Assess the morphology of the erythrocytes.
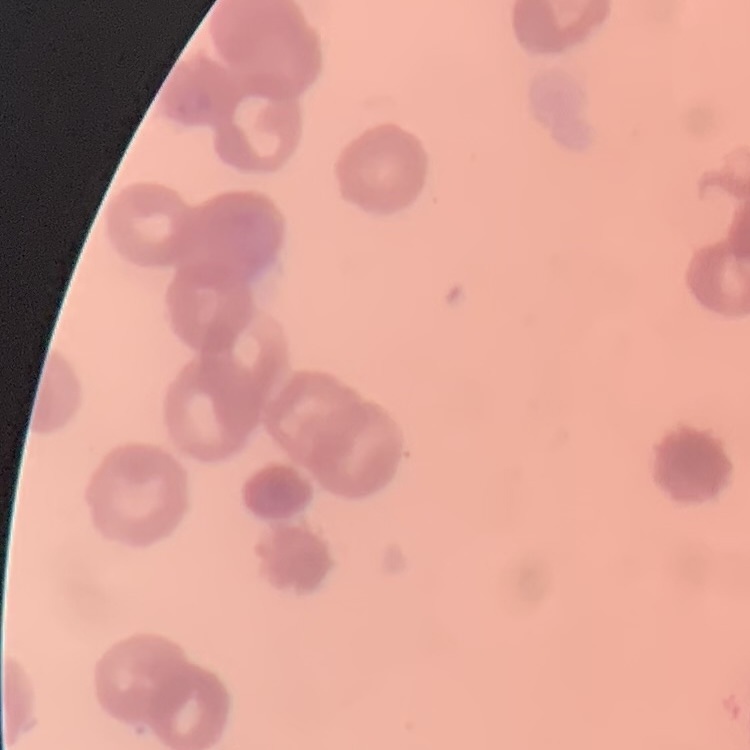

They show rouleaux formation.

One tile cut from a larger photomicrograph. Field's or Giemsa stain. Thin blood film.